Describe the morphology of the red blood cells.
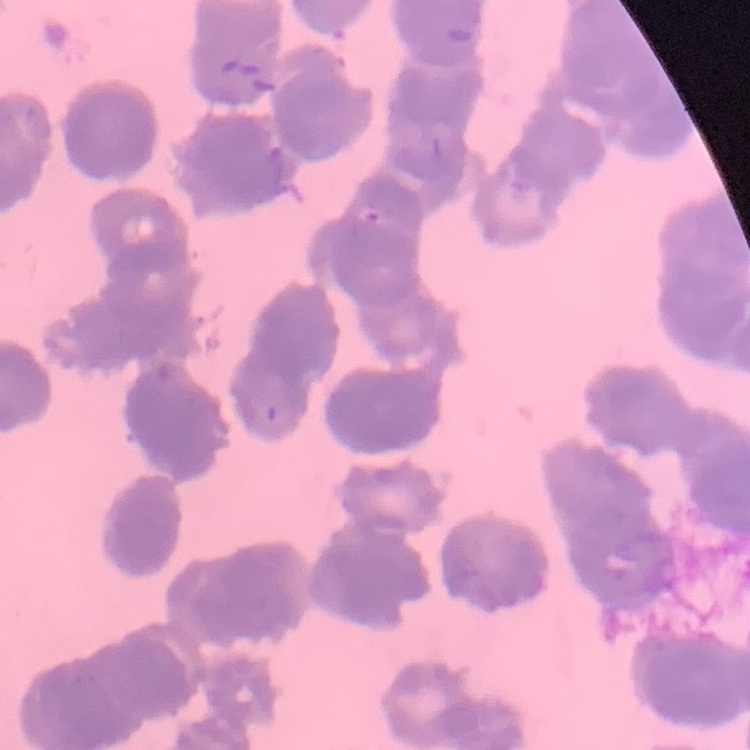

Rouleaux formation.

stain = Field's or Giemsa
preparation = thin peripheral smear
image type = one tile cut from a larger photomicrograph